Evaluate for Plasmodium parasites.
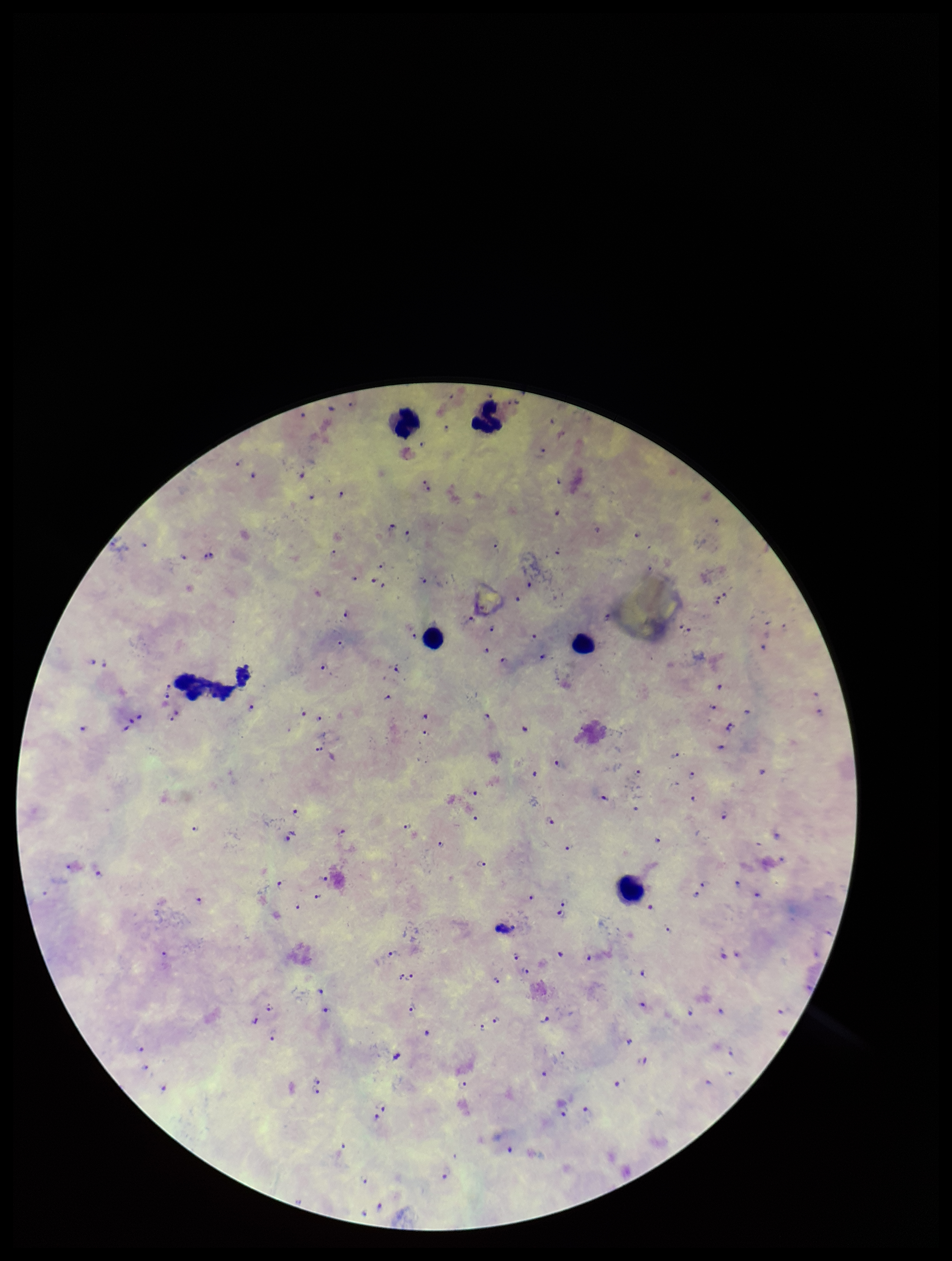
Detected.

leukocyte count = 6
stain = Giemsa
capture = smartphone photograph through the microscope eyepiece
field of view = single
image size = 952×1261 pixels
preparation = thick blood smear
species reported for this patient = Plasmodium falciparum
parasite count = 117
patient malaria status = positive